Classify this cell by malaria status.
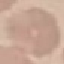
Uninfected.

Summary:
  - Stain: Giemsa
  - Capture: smartphone camera at the microscope eyepiece
  - Image type: automatically extracted cell patch, resized to 64 × 64 pixels
  - Preparation: thin blood smear